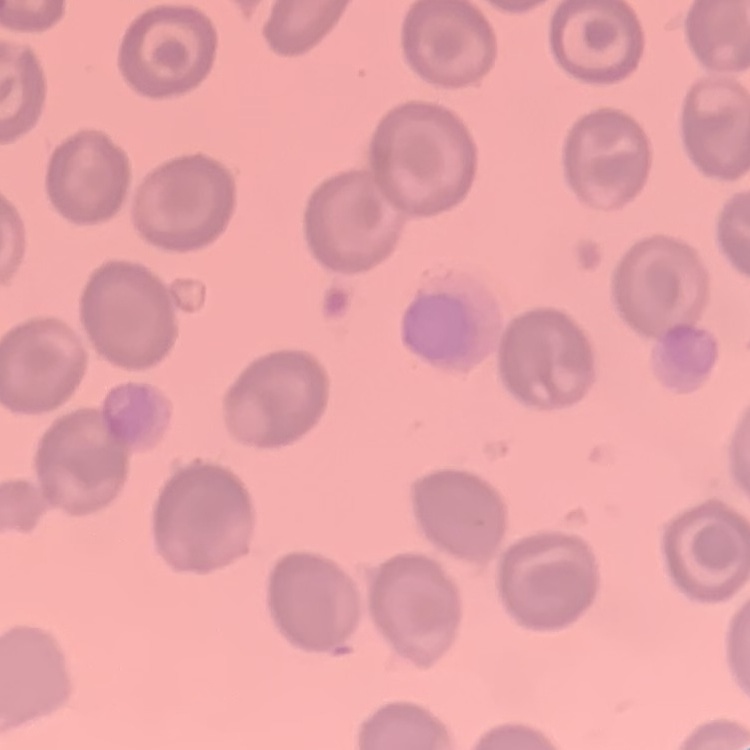

Summary:
  - Red blood cell morphology: no rouleaux formation
  - Image type: square crop of a larger photomicrograph
  - Stain: Field's or Giemsa
  - Preparation: thin blood film